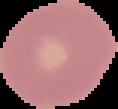
From a thin blood smear. Cell region segmented out of the field of view; the surrounding area is masked to black. Malaria status: uninfected. Image is 118×109 pixels.